Classify this cell by malaria status.
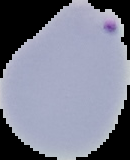

Parasitized.

Segmented cell region on a black background. From a thin blood smear. Image is 130×160 pixels.